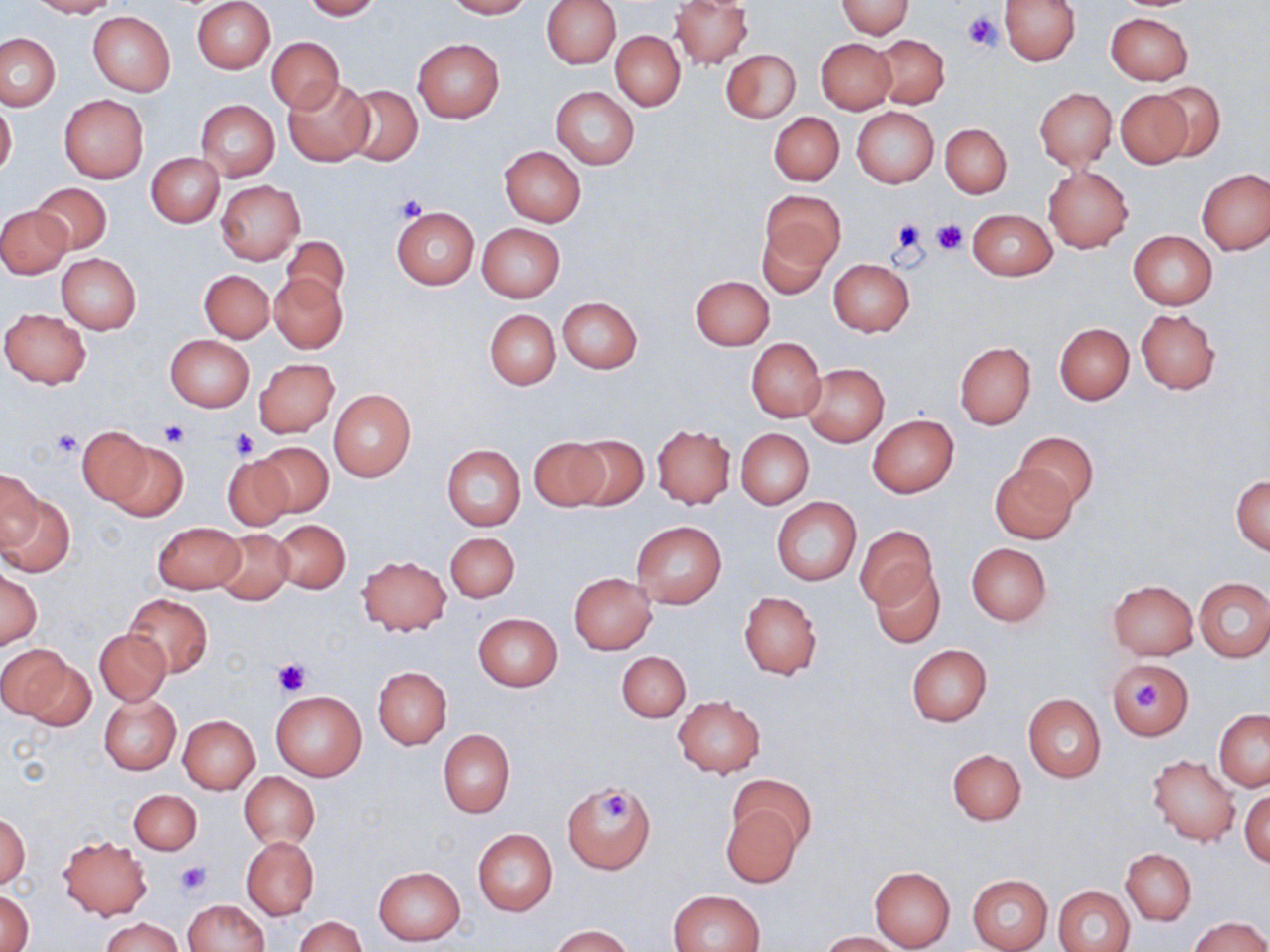
Summary:
  - Coordinate format: approximate bounding boxes as (x1,y1)-(x2,y2) corner pairs in pixels
  - Platelet locations: (963,12)-(1004,54), (393,195)-(427,223), (890,219)-(925,257), (931,219)-(969,255), (158,419)-(192,445), (51,428)-(83,458), (230,428)-(257,459), (273,658)-(309,696), (1134,683)-(1161,710), (603,794)-(631,821), (175,862)-(210,895)
  - Uninfected red blood cell locations: (26,0)-(116,18), (301,0)-(381,20), (443,0)-(531,18), (672,0)-(753,68), (837,0)-(914,37), (999,0)-(1080,65), (192,1)-(274,74), (541,1)-(620,68), (87,11)-(175,96), (1105,12)-(1192,86), (611,31)-(684,110), (0,33)-(60,111), (874,34)-(949,109), (266,37)-(344,112), (413,38)-(504,122), (816,39)-(896,114), (721,50)-(801,123), (283,79)-(373,165), (1151,82)-(1226,163), (344,86)-(422,166), (551,87)-(639,169), (1034,87)-(1116,170), (1115,88)-(1192,167), (59,95)-(149,183), (0,99)-(17,180), (196,100)-(280,181), (852,107)-(938,187), (769,112)-(844,185), (940,123)-(1011,197), (157,129)-(245,212), (499,146)-(586,226), (147,152)-(224,226), (1043,166)-(1133,253), (1197,169)-(1269,255), (216,179)-(304,266), (30,183)-(111,255), (762,189)-(845,274), (1,206)-(75,355), (390,206)-(480,290), (1,207)-(70,278), (968,208)-(1057,281), (757,220)-(836,299), (477,223)-(565,302), (1129,230)-(1217,309), (280,235)-(350,307), (56,253)-(142,334), (828,259)-(915,335), (190,270)-(267,406), (200,270)-(274,343), (270,273)-(347,352), (691,276)-(774,349), (557,296)-(643,375), (1,308)-(91,388), (485,309)-(560,389), (1136,309)-(1220,394), (1054,322)-(1134,404), (165,335)-(253,412), (746,339)-(825,420), (955,342)-(1035,428), (254,359)-(340,438), (802,363)-(888,447), (328,389)-(416,482), (868,415)-(959,498), (653,425)-(736,508), (73,426)-(156,510), (735,428)-(813,508), (1015,432)-(1098,509), (565,435)-(650,513), (528,437)-(611,514), (106,438)-(187,520), (254,442)-(334,517), (442,444)-(526,530), (223,455)-(297,529), (991,463)-(1078,543), (2,469)-(42,554), (1232,474)-(1270,556), (0,485)-(73,580), (772,497)-(861,585), (274,520)-(350,593), (630,520)-(727,609), (153,522)-(245,594), (854,526)-(936,612), (213,529)-(293,603), (445,532)-(519,602), (966,543)-(1052,626), (357,555)-(450,636), (869,565)-(944,647), (0,567)-(41,649), (569,572)-(657,653), (1194,577)-(1270,662), (1107,580)-(1198,660), (739,591)-(822,679), (124,594)-(213,678), (473,613)-(563,692), (95,627)-(170,705), (907,645)-(992,726), (2,646)-(83,725), (616,651)-(691,722), (1108,659)-(1194,740), (373,666)-(452,749), (271,689)-(366,782), (1023,693)-(1107,783), (99,695)-(180,774), (673,695)-(765,778), (1214,710)-(1270,791), (177,715)-(260,794), (438,729)-(515,816), (948,750)-(1025,825), (1147,754)-(1240,846), (240,772)-(319,849), (728,774)-(814,858), (562,781)-(654,873), (1240,789)-(1269,866), (129,790)-(201,854), (720,803)-(804,886), (0,812)-(30,888), (472,829)-(557,916), (59,836)-(152,919), (242,836)-(318,919), (1121,849)-(1196,923), (868,865)-(956,952), (372,866)-(465,946), (967,874)-(1053,952), (1054,886)-(1135,952), (670,889)-(765,952), (1,890)-(34,951), (183,899)-(270,951), (101,916)-(181,952), (294,916)-(365,952), (1190,916)-(1269,952), (552,925)-(632,952), (821,932)-(902,952)
  - Slide-level diagnosis: no evidence of blood parasites
  - Preparation: thin blood film
  - Image size: 1270×952 pixels
  - Stain: May-Grünwald-Giemsa
  - Modality: optical microscopy
  - Field of view: single
  - Magnification: 1000x